Assess this cell for malaria.
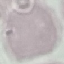

It is uninfected.

{
  "capture": "smartphone camera at the microscope eyepiece",
  "preparation": "thin blood film",
  "stain": "Giemsa",
  "image_type": "cell patch, automatically extracted from a larger field of view and resized to 64 × 64 pixels"
}